Classify this cell by malaria status.
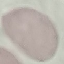
Uninfected.

Summary:
  - Preparation: thin blood smear
  - Capture: smartphone camera at the microscope eyepiece
  - Stain: Giemsa
  - Image type: cell patch, automatically extracted from a larger field of view and resized to 64 × 64 pixels